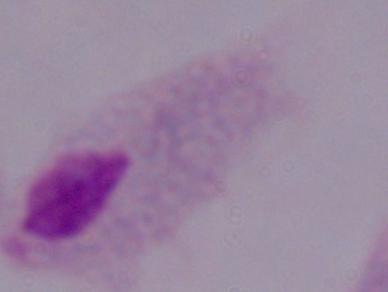

Photomicrograph. 1000x magnification. A trichomonad is seen.